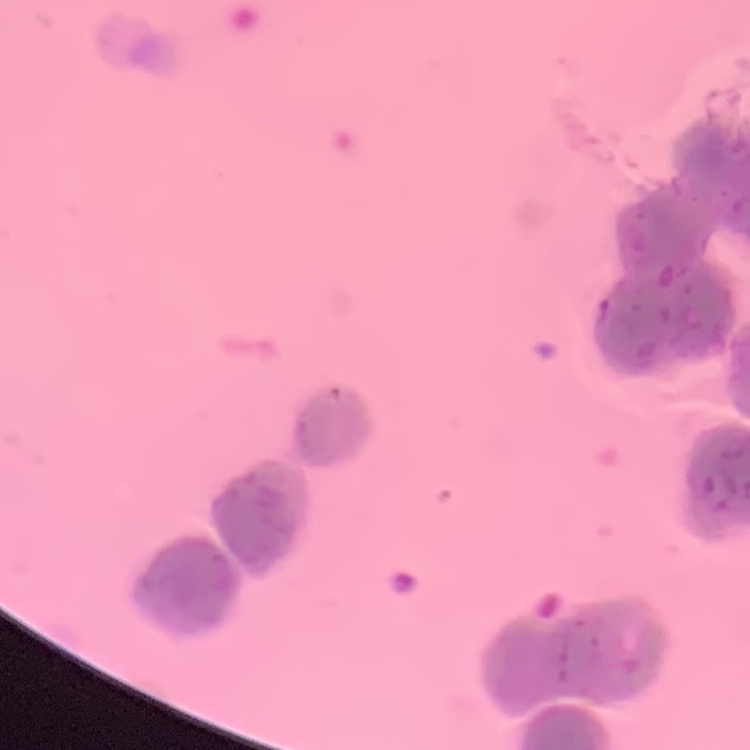
The erythrocytes show rouleaux formation. Stained with either Field's or Giemsa. Thin blood smear. Square crop of a larger photomicrograph.